Report the malaria status of this cell.
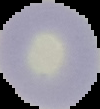

It is uninfected.

image type = segmented cell region with the area outside set to black
image size = 100×109 pixels
preparation = thin blood smear